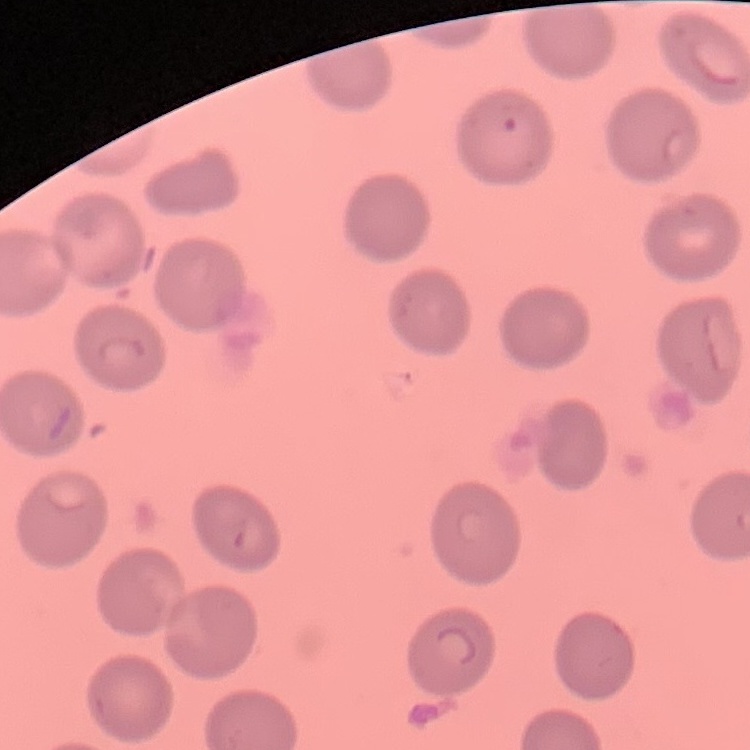 The erythrocytes exhibit no rouleaux formation. Thin blood film. One tile cut from a larger photomicrograph. Field's or Giemsa stain.